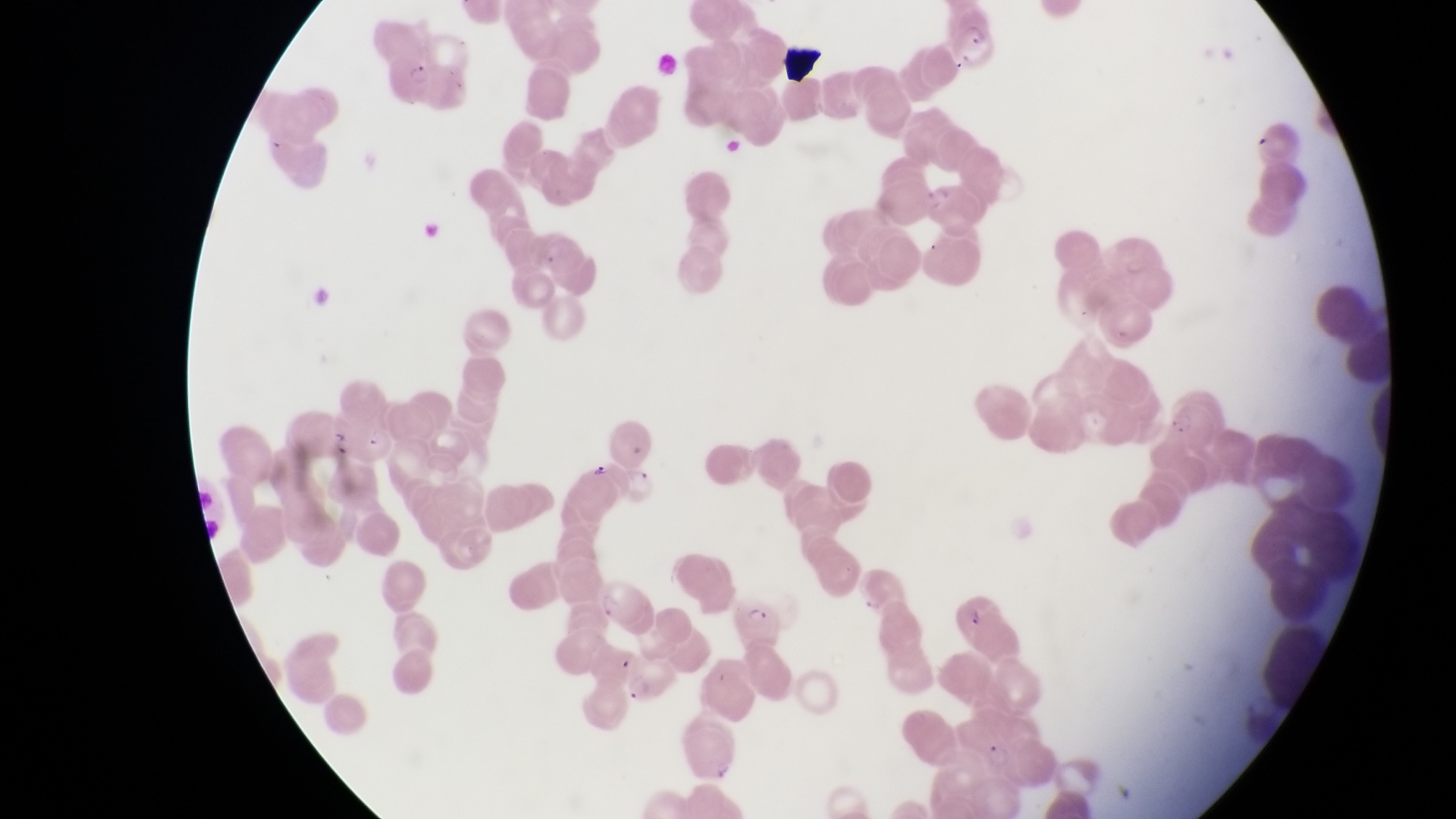

Approximate bounding boxes as [left, top, right, bottom] in pixels. Artifact (platelet-like body, stain precipitate, or debris) locations: [781, 40, 826, 86], [327, 422, 354, 459]. Parasitised red blood cell locations: [946, 8, 999, 74], [389, 46, 442, 106], [595, 579, 651, 628], [949, 587, 1010, 643], [733, 591, 786, 647], [626, 660, 679, 705]. Trophozoite locations: [594, 460, 613, 483]. Photographed through the eyepiece of an Olympus CX-23 microscope with a smartphone camera. Sample from Uganda. Magnification of 1000x. Image is 1456×819 pixels. Single field of view. Thin blood film.